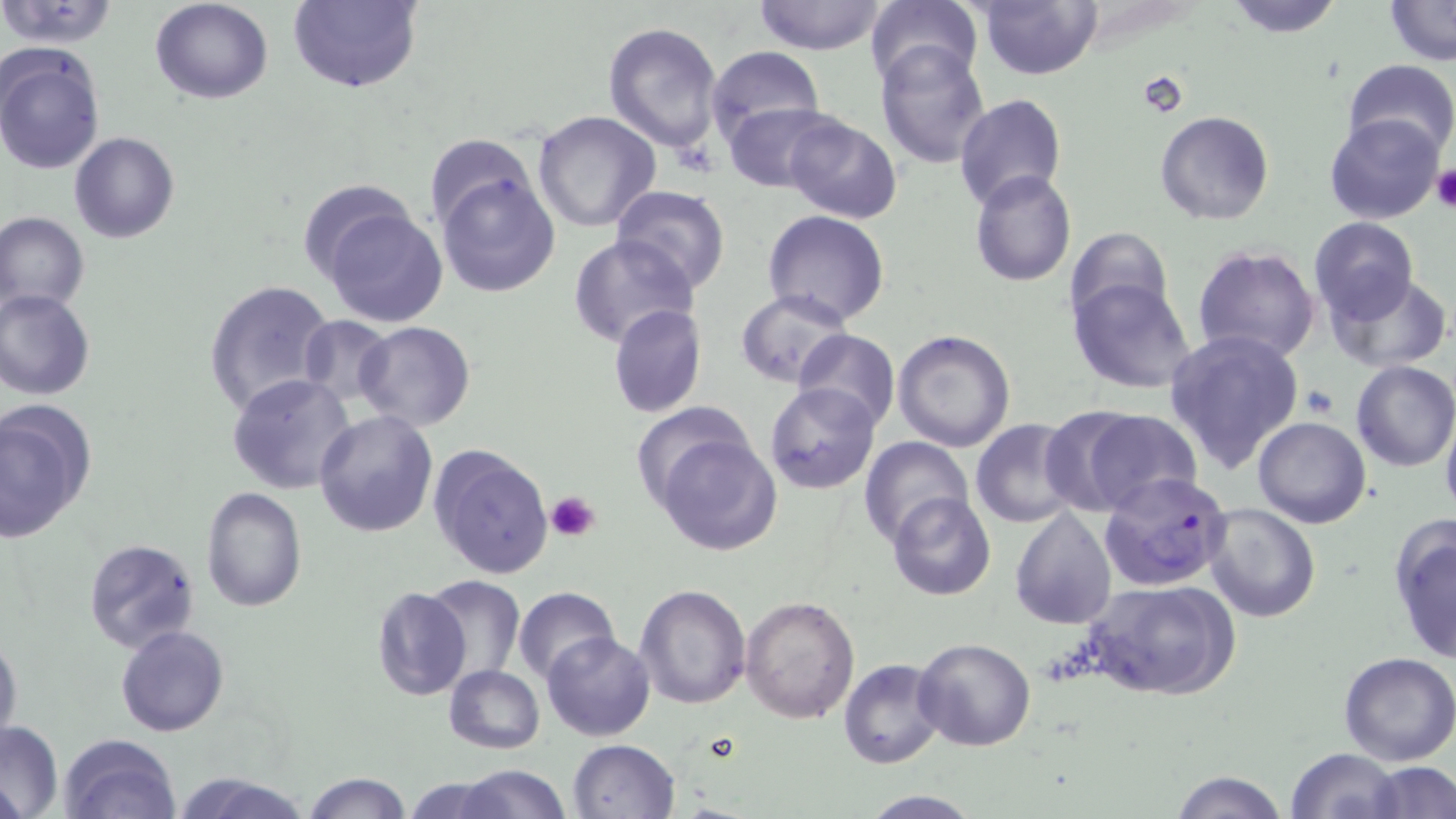 Approximate bounding boxes as (x1,y1)-(x2,y2) corner pairs in pixels. Uninfected red blood cell locations: (150,0)-(273,104), (751,0)-(889,55), (864,0)-(982,92), (977,0)-(1102,79), (1222,0)-(1346,38), (1382,0)-(1455,66), (0,1)-(122,50), (286,1)-(424,93), (602,22)-(726,153), (876,41)-(992,166), (0,42)-(106,175), (704,46)-(825,148), (1341,58)-(1455,163), (953,92)-(1068,210), (725,103)-(838,193), (533,110)-(661,232), (1154,111)-(1274,225), (781,113)-(903,223), (1323,113)-(1444,225), (68,133)-(179,243), (425,137)-(543,234), (434,166)-(560,298), (970,171)-(1076,288), (297,180)-(422,287), (609,183)-(730,291), (320,200)-(447,328), (763,210)-(890,328), (0,212)-(89,317), (1309,217)-(1419,324), (1064,227)-(1175,333), (568,234)-(697,348), (1190,245)-(1321,366), (1326,273)-(1453,372), (1067,277)-(1198,394), (204,278)-(335,419), (0,288)-(97,400), (735,289)-(854,389), (609,303)-(707,417), (298,314)-(395,411), (354,322)-(477,431), (794,329)-(900,432), (892,329)-(1017,451), (1163,329)-(1305,475), (1351,359)-(1456,471), (227,373)-(355,495), (764,383)-(882,496), (633,399)-(762,511), (0,401)-(96,546), (1066,406)-(1204,515), (313,408)-(439,538), (1440,410)-(1456,521), (1253,417)-(1371,529), (971,419)-(1085,527), (652,432)-(782,556), (861,437)-(974,547), (429,442)-(555,581), (200,487)-(307,613), (887,492)-(996,601), (1201,501)-(1323,622), (1010,508)-(1116,628), (1387,514)-(1456,666), (81,538)-(201,655), (422,576)-(525,685), (1083,578)-(1239,703), (634,584)-(752,710), (372,585)-(471,700), (513,586)-(621,685), (739,594)-(861,723), (115,624)-(230,737), (542,631)-(655,741), (0,632)-(23,749), (913,637)-(1036,751), (1337,651)-(1456,765), (839,659)-(945,769), (444,664)-(545,753), (0,720)-(62,818), (57,734)-(182,819), (568,738)-(681,819), (1283,748)-(1404,819), (1367,761)-(1456,818), (453,765)-(570,819), (1168,769)-(1289,819), (173,772)-(313,818), (304,773)-(412,818), (402,775)-(514,818), (856,791)-(985,818). Platelet locations: (1432,166)-(1456,212), (1302,386)-(1337,418), (547,489)-(602,542). Plasmodium falciparum-infected red blood cell locations: (1101,470)-(1232,592). Slide-level diagnosis: Plasmodium falciparum. 1000x magnification. Light microscopy. Single field of view. Image is 1456×819 pixels. Thin blood smear. May-Grünwald-Giemsa stain.